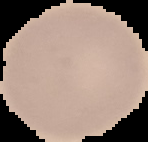 Image is 148×142 pixels. Cell region segmented out of the field of view; the surrounding area is masked to black. From a thin blood smear. Malaria status: uninfected.